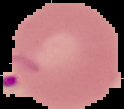
image type = cell region segmented out of the field of view; surrounding area masked to black
image size = 124×109 pixels
result = Plasmodium parasites identified
preparation = thin blood smear